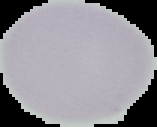

Image is 157×127 pixels. From a thin blood smear. The area outside the segmented cell region is set to black. Result: no Plasmodium parasites detected.